Classify this cell by malaria status.
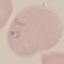
It is parasitized.

Summary:
  - Image type: automatically extracted cell patch, resized to 64 × 64 pixels
  - Preparation: thin blood smear
  - Capture: smartphone camera at the microscope eyepiece
  - Stain: Giemsa